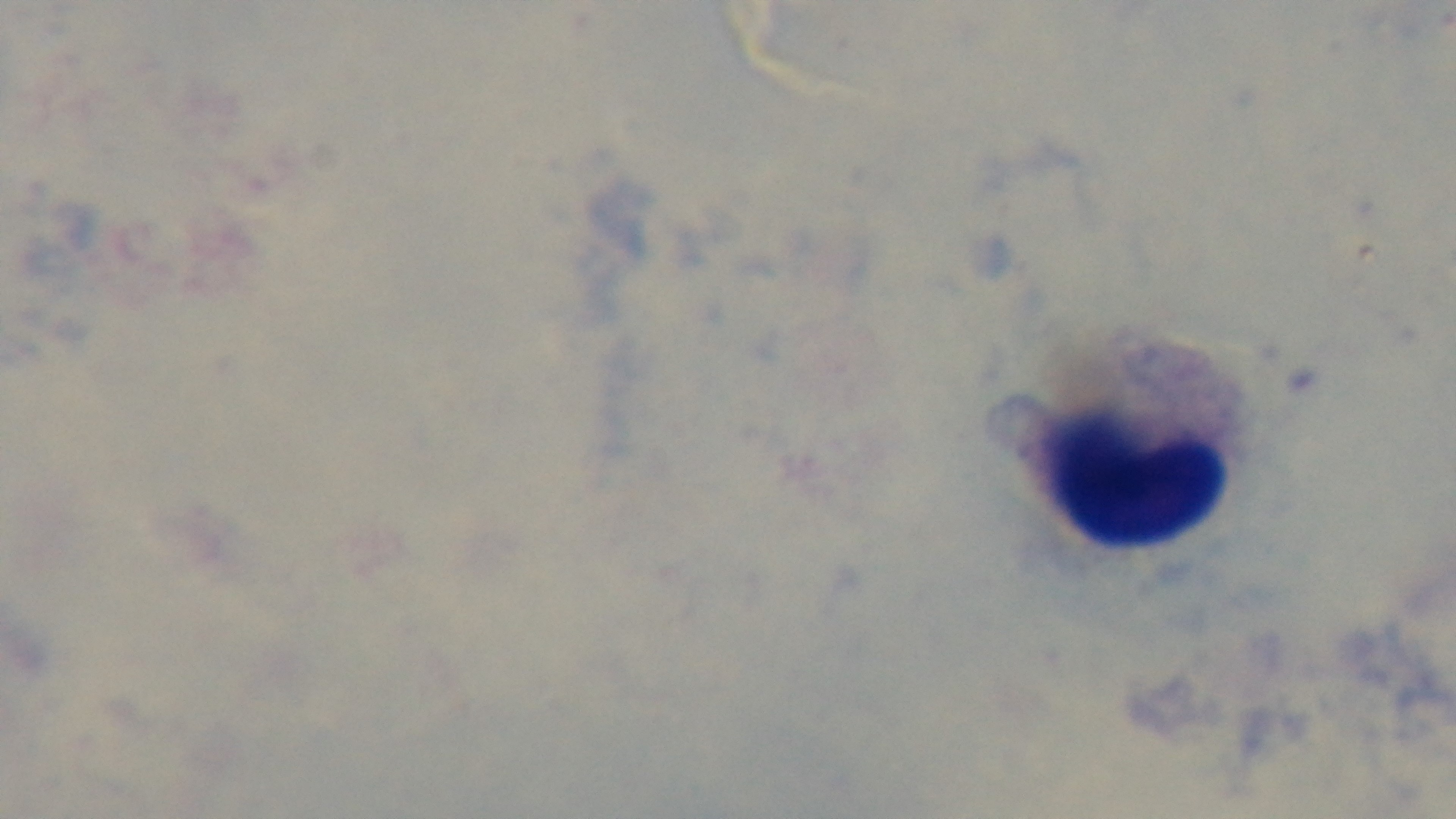

field of view = single
malaria status = uninfected
preparation = thick
capture = mounted 4K digital camera
modality = light microscopy
objective = 100x oil immersion
stain = Giemsa